Assess the morphology of the erythrocytes.
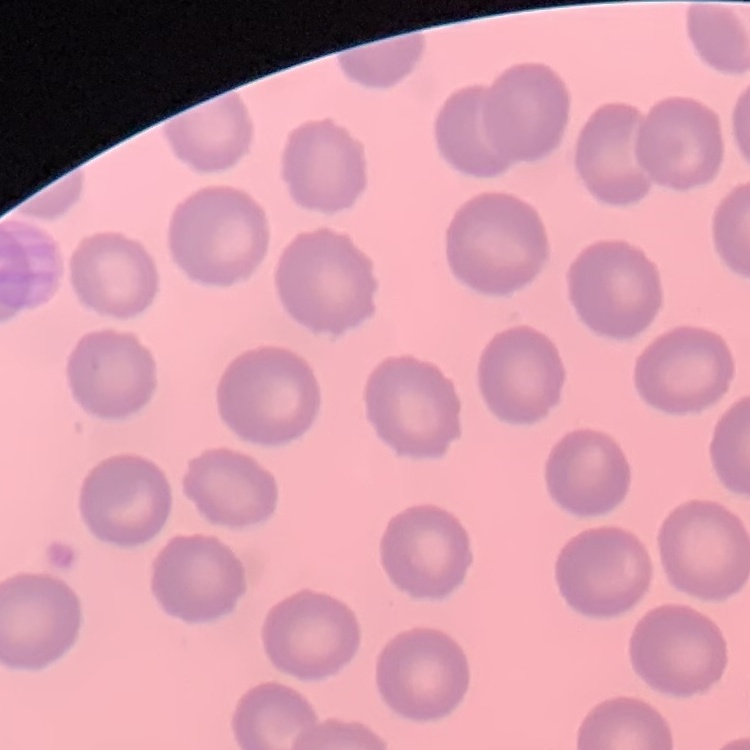

They show no rouleaux formation.

Square crop of a larger photomicrograph. Thin peripheral smear. Field's or Giemsa stain.